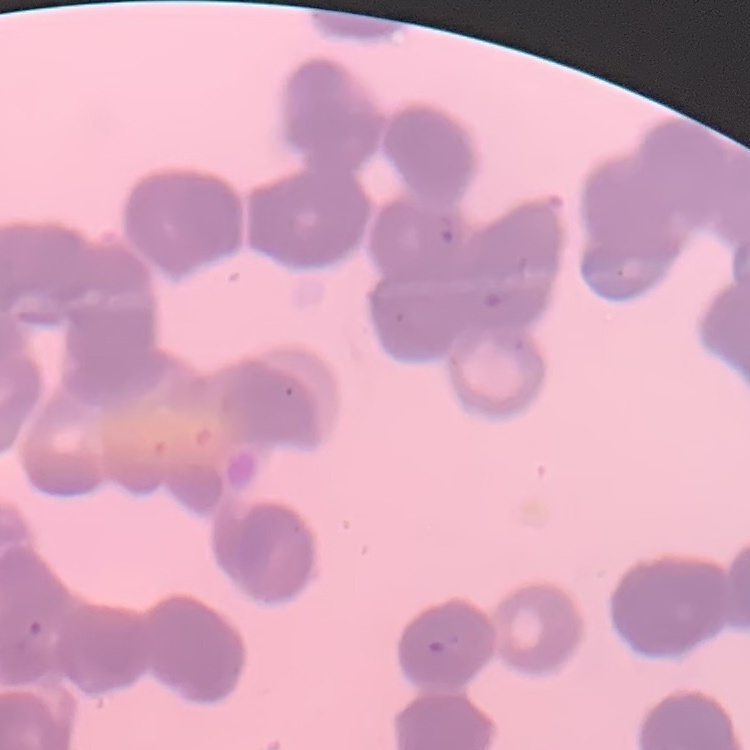
{
  "red_blood_cell_morphology": "rouleaux formation",
  "image_type": "one tile cut from a larger photomicrograph",
  "stain": "Field's or Giemsa",
  "preparation": "thin peripheral smear"
}